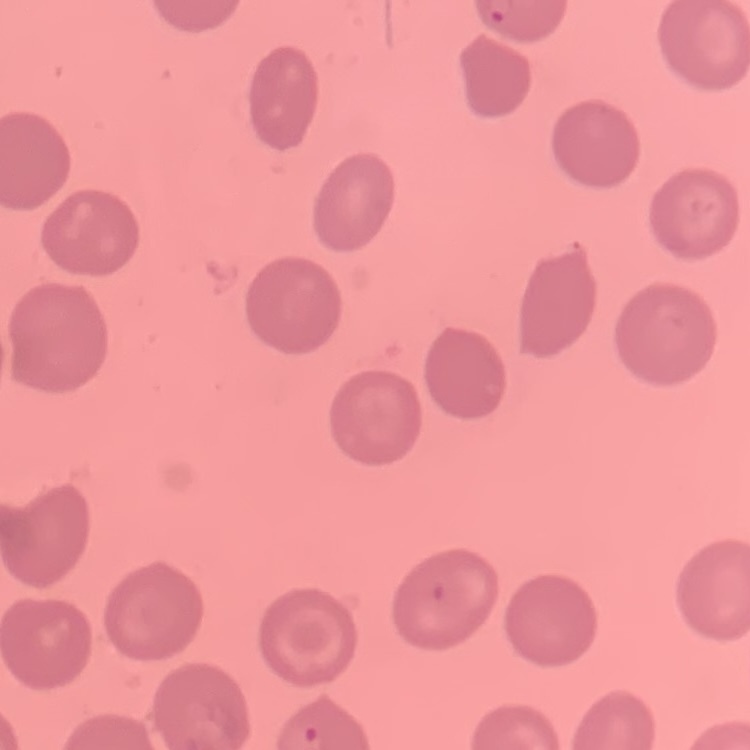

The erythrocytes exhibit no rouleaux formation. One tile cut from a larger photomicrograph. Stained with either Field's or Giemsa. Thin blood smear.